Outline every Plasmodium parasite.
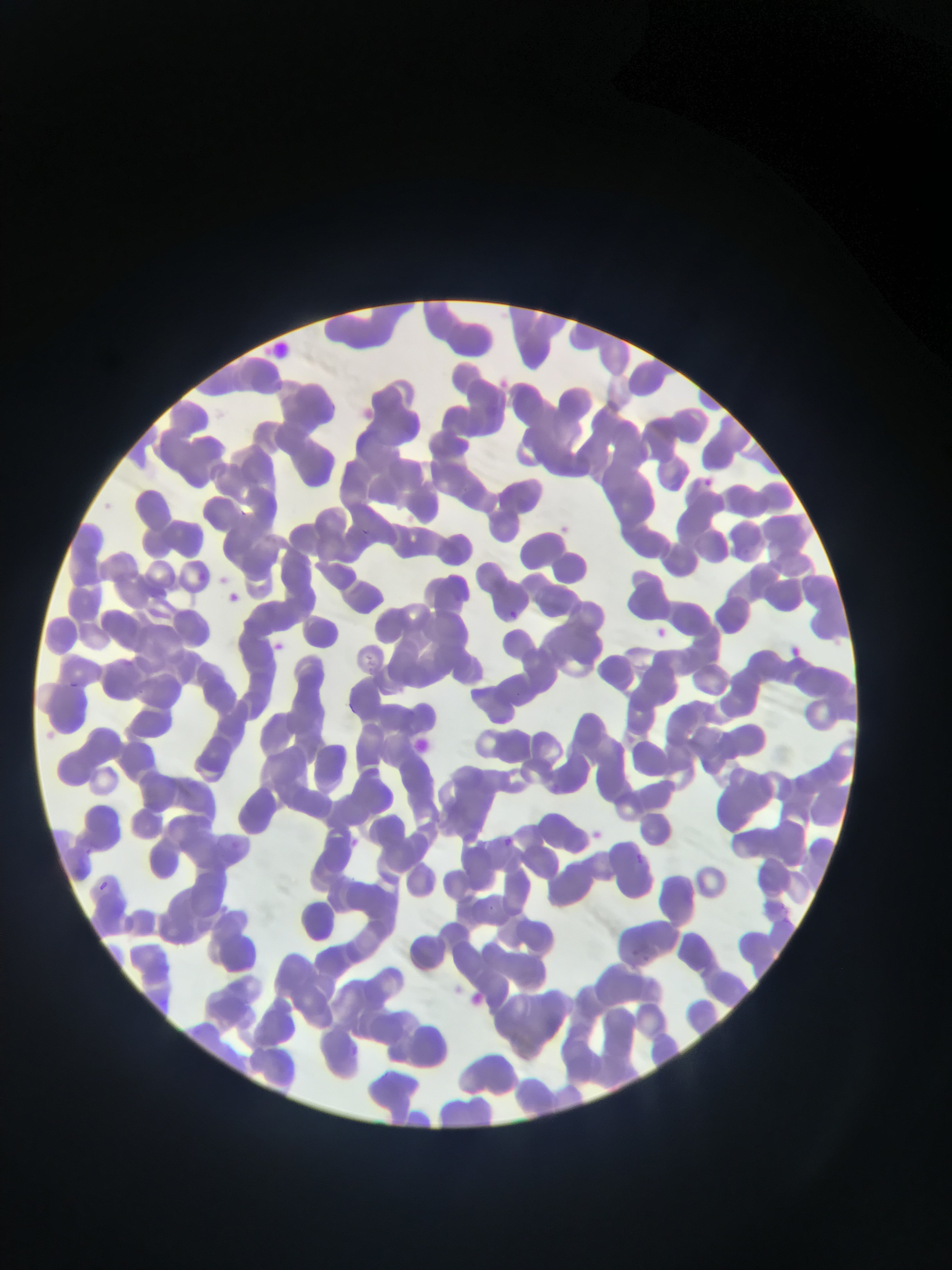
Approximate bounding boxes as {left, top, right, bottom} in pixels.
Plasmodium parasites: {366, 653, 374, 672}, {629, 949, 653, 965}.

Sample from Ghana. Thin blood film. Image is 952×1270 pixels. One field of view. Mobile-phone photograph taken through the microscope.